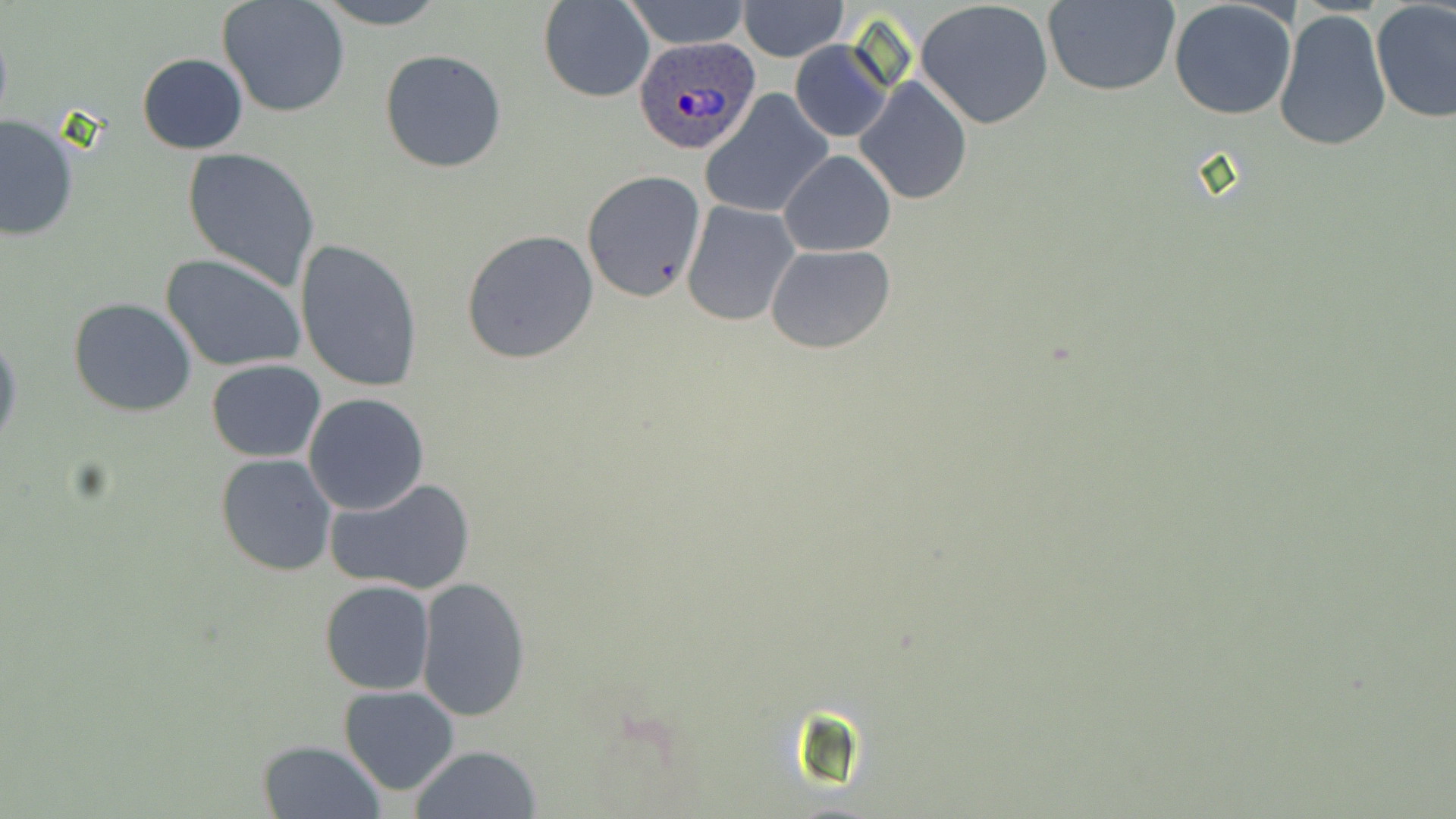

Approximate bounding boxes as named x1/y1/x2/y2 corners in pixels. Plasmodium ovale-infected red blood cell locations: (x1=633, y1=35, x2=764, y2=155). Uninfected red blood cell locations: (x1=312, y1=0, x2=447, y2=29), (x1=539, y1=0, x2=655, y2=102), (x1=622, y1=0, x2=751, y2=49), (x1=1044, y1=0, x2=1179, y2=97), (x1=1169, y1=0, x2=1297, y2=119), (x1=217, y1=1, x2=349, y2=118), (x1=737, y1=1, x2=849, y2=63), (x1=915, y1=1, x2=1056, y2=129), (x1=1370, y1=3, x2=1456, y2=123), (x1=1273, y1=9, x2=1392, y2=153), (x1=790, y1=39, x2=893, y2=143), (x1=380, y1=49, x2=507, y2=172), (x1=136, y1=53, x2=248, y2=154), (x1=856, y1=76, x2=971, y2=205), (x1=702, y1=92, x2=831, y2=218), (x1=0, y1=114, x2=80, y2=241), (x1=182, y1=148, x2=321, y2=289), (x1=779, y1=150, x2=895, y2=257), (x1=581, y1=169, x2=707, y2=303), (x1=681, y1=201, x2=800, y2=326), (x1=461, y1=229, x2=599, y2=364), (x1=294, y1=238, x2=424, y2=393), (x1=765, y1=243, x2=895, y2=352), (x1=161, y1=255, x2=305, y2=373), (x1=68, y1=298, x2=197, y2=418), (x1=0, y1=332, x2=21, y2=458), (x1=207, y1=358, x2=326, y2=462), (x1=303, y1=392, x2=430, y2=515), (x1=214, y1=454, x2=339, y2=576), (x1=325, y1=477, x2=477, y2=597), (x1=414, y1=576, x2=532, y2=723), (x1=319, y1=580, x2=435, y2=696), (x1=338, y1=684, x2=461, y2=795), (x1=272, y1=715, x2=453, y2=812), (x1=257, y1=740, x2=385, y2=819), (x1=408, y1=745, x2=544, y2=819). Slide-level diagnosis: Plasmodium ovale. Captured at 1000x magnification. May-Grünwald-Giemsa stain. Thin blood smear. Image is 1456×819 pixels. Light microscopy. One field of a larger specimen.